Report the malaria status of this cell.
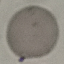
It is uninfected.

Summary:
  - Image type: cell patch, automatically extracted from a larger field of view and resized to 64 × 64 pixels
  - Capture: smartphone through the microscope eyepiece
  - Stain: Giemsa
  - Preparation: thin smear